Assess this cell for malaria.
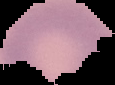

Parasitized.

Summary:
  - Preparation: thin blood smear
  - Image size: 115×85 pixels
  - Image type: segmented cell region on a black background